Report the malaria status of this cell.
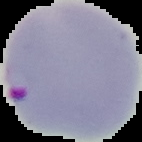
Parasitized.

preparation = thin blood smear
image size = 142×142 pixels
image type = segmented cell region with the area outside set to black